Locate every cell, classifying each as a parasitized RBC, an uninfected RBC, or a WBC.
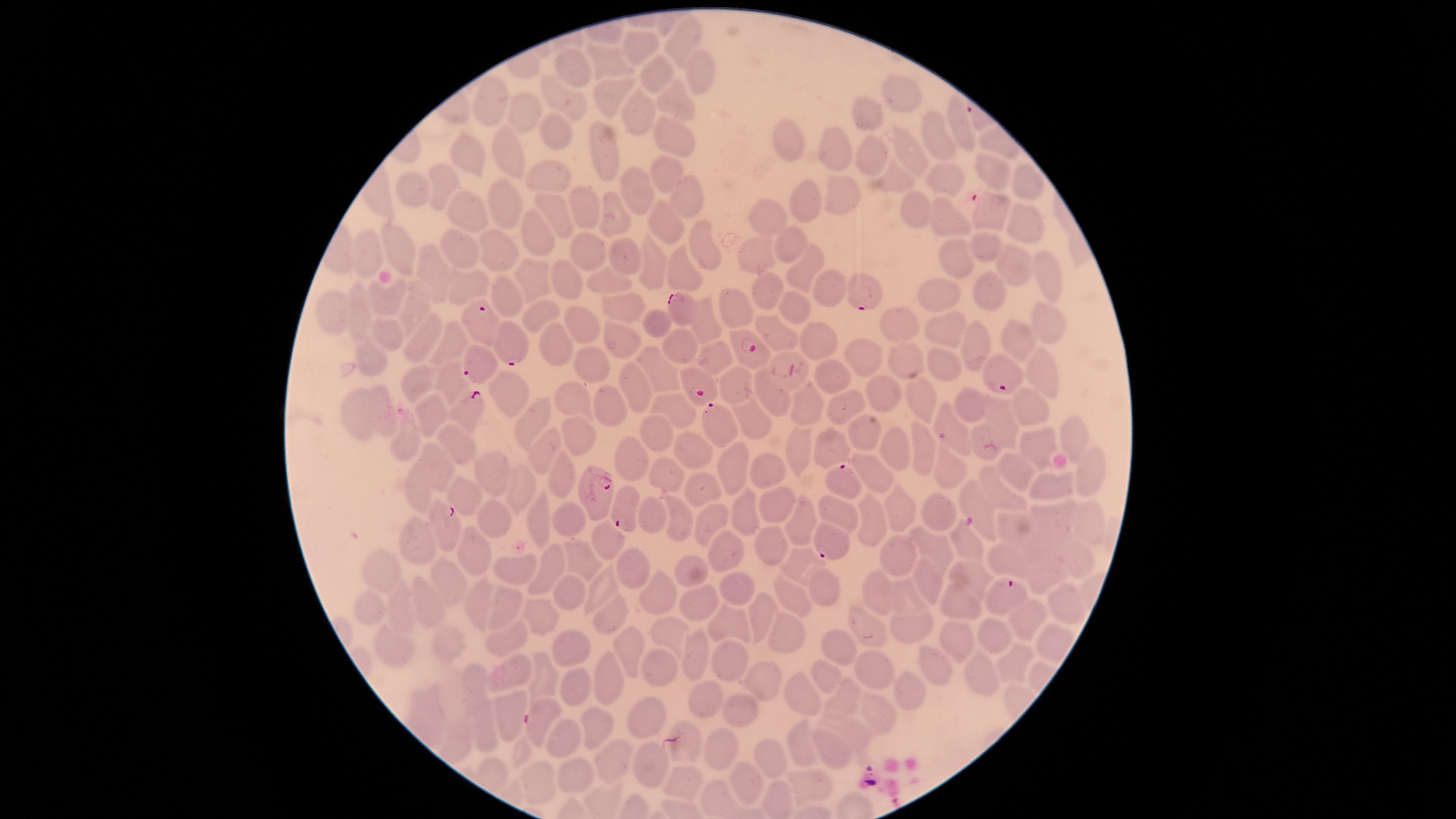

Approximate bounding boxes as (left, top, right, bottom) in pixels.
Parasitized RBCs: (845, 273, 883, 310), (666, 292, 697, 327), (461, 299, 500, 347), (493, 319, 528, 366), (729, 329, 771, 370), (462, 344, 498, 384), (982, 353, 1025, 394), (679, 365, 718, 406), (445, 390, 485, 434), (702, 403, 739, 448), (578, 464, 614, 521), (824, 464, 862, 500), (610, 486, 640, 532), (426, 498, 461, 551), (812, 522, 851, 560), (984, 578, 1028, 615), (524, 696, 563, 748).
Uninfected RBCs: (664, 15, 705, 69), (623, 30, 661, 67), (584, 42, 637, 83), (554, 48, 592, 88), (682, 49, 716, 96), (639, 52, 675, 94), (540, 71, 588, 122), (881, 72, 922, 113), (472, 73, 509, 128), (653, 75, 696, 122), (592, 77, 639, 119), (620, 84, 658, 136), (505, 91, 544, 136), (852, 95, 885, 131), (948, 95, 976, 151), (921, 109, 955, 160), (538, 111, 573, 150), (652, 114, 696, 157), (771, 118, 806, 162), (589, 120, 622, 182), (490, 122, 524, 179), (817, 124, 852, 171), (891, 124, 930, 178), (448, 129, 487, 181), (855, 132, 890, 176), (976, 151, 1012, 191), (648, 154, 685, 193), (875, 157, 916, 194), (524, 159, 572, 191), (924, 160, 966, 197), (427, 161, 461, 211), (1010, 162, 1047, 200), (619, 167, 655, 215), (395, 170, 432, 208), (823, 173, 861, 214), (669, 174, 704, 219), (789, 177, 823, 222), (486, 178, 522, 229), (567, 184, 602, 229), (972, 188, 1011, 231), (445, 189, 489, 234), (900, 189, 933, 229), (533, 191, 574, 238), (599, 191, 632, 236), (930, 195, 973, 238), (648, 199, 686, 246), (748, 199, 787, 237), (1006, 201, 1045, 246), (519, 207, 557, 255), (689, 219, 724, 271), (380, 222, 416, 276), (773, 224, 809, 264), (439, 227, 481, 268), (478, 227, 518, 273), (638, 227, 669, 290), (349, 228, 384, 279), (569, 229, 608, 270), (968, 229, 1004, 262), (736, 234, 777, 274), (607, 238, 642, 276), (938, 238, 975, 279), (993, 241, 1035, 287), (415, 242, 452, 305), (666, 243, 704, 291), (784, 243, 825, 294), (1033, 250, 1063, 305), (512, 256, 554, 304), (550, 259, 584, 299), (585, 264, 633, 294), (448, 266, 491, 306), (812, 268, 847, 307), (750, 270, 786, 309), (972, 270, 1008, 312), (490, 274, 525, 317), (366, 277, 408, 318), (396, 277, 431, 342), (917, 277, 961, 312), (345, 278, 371, 343), (718, 286, 755, 328), (315, 290, 353, 336), (600, 290, 649, 325), (777, 290, 811, 326), (690, 293, 723, 346), (521, 300, 561, 333), (1031, 301, 1068, 344), (879, 304, 919, 341), (564, 305, 600, 343), (401, 308, 443, 367), (643, 308, 674, 338), (925, 311, 969, 349), (754, 313, 800, 352), (368, 318, 403, 352), (960, 318, 992, 373), (1001, 318, 1038, 363), (424, 319, 470, 369), (603, 319, 642, 359), (799, 320, 838, 361), (538, 321, 573, 367), (661, 327, 700, 365), (354, 330, 389, 377), (843, 338, 883, 378), (886, 339, 924, 379), (693, 340, 734, 374), (927, 344, 963, 383), (633, 345, 682, 393), (573, 346, 609, 382), (1025, 346, 1062, 399), (767, 350, 812, 390), (433, 357, 470, 410), (812, 358, 851, 394), (617, 360, 654, 412), (400, 363, 435, 404), (717, 365, 755, 404), (752, 367, 792, 417), (486, 369, 530, 418), (866, 374, 903, 414), (904, 374, 940, 425), (790, 379, 826, 425), (553, 380, 594, 423), (362, 384, 397, 437), (592, 384, 628, 428), (1012, 386, 1050, 428), (952, 387, 989, 423), (339, 388, 387, 441), (414, 390, 447, 436), (826, 390, 865, 424), (649, 392, 698, 430), (982, 392, 1020, 450), (515, 395, 551, 453), (731, 395, 772, 440), (932, 401, 972, 457), (847, 413, 881, 451), (639, 415, 675, 454), (1058, 415, 1090, 463), (561, 416, 598, 459), (911, 420, 938, 476), (969, 421, 1003, 461), (390, 422, 421, 460), (435, 422, 477, 465), (527, 425, 562, 475), (1018, 425, 1058, 470), (784, 426, 814, 478), (813, 426, 851, 470), (878, 426, 911, 471), (673, 430, 714, 471), (615, 433, 651, 483), (717, 439, 749, 497), (419, 440, 456, 494), (933, 442, 968, 489), (1076, 445, 1107, 498), (546, 446, 578, 500), (474, 449, 512, 497), (998, 451, 1035, 492), (749, 452, 786, 489), (850, 453, 894, 494), (648, 457, 686, 493), (403, 461, 434, 512), (505, 463, 537, 515), (978, 464, 1029, 512), (684, 470, 722, 508), (1027, 470, 1074, 500), (445, 475, 484, 517), (884, 479, 917, 532), (959, 479, 998, 543), (729, 485, 760, 535), (758, 486, 796, 524), (526, 489, 551, 552), (856, 489, 888, 547), (784, 491, 818, 545), (920, 492, 959, 532), (664, 493, 695, 542), (636, 495, 667, 534), (816, 495, 860, 534), (477, 498, 513, 538), (550, 501, 588, 537), (1030, 501, 1076, 545), (1071, 501, 1106, 547), (693, 502, 731, 548), (997, 511, 1037, 546), (398, 516, 436, 566), (591, 518, 626, 562), (948, 519, 986, 563), (456, 524, 493, 575), (908, 524, 954, 577), (754, 525, 790, 565), (708, 529, 745, 573), (880, 534, 919, 577), (1061, 537, 1096, 580), (563, 539, 604, 584), (987, 540, 1030, 580), (526, 542, 567, 597), (779, 545, 829, 589), (615, 546, 651, 589), (361, 548, 403, 594), (492, 552, 538, 586), (1028, 552, 1070, 595), (674, 554, 709, 588), (912, 554, 942, 606), (428, 555, 467, 607), (948, 559, 995, 601), (584, 560, 619, 615), (638, 567, 679, 614), (862, 567, 894, 616), (807, 568, 840, 607), (552, 571, 588, 613), (719, 571, 755, 606), (773, 571, 813, 617), (462, 573, 491, 633), (412, 575, 445, 628), (384, 576, 418, 635), (887, 576, 931, 613), (938, 579, 984, 620), (487, 581, 526, 632), (679, 583, 720, 621), (1046, 583, 1086, 626), (354, 590, 387, 625), (592, 592, 628, 636), (746, 592, 780, 646), (1008, 597, 1047, 640), (521, 598, 560, 636), (706, 600, 752, 643), (847, 604, 888, 649), (889, 610, 935, 643), (766, 612, 807, 654), (650, 615, 691, 660), (977, 616, 1013, 654), (484, 618, 529, 660), (938, 618, 976, 662), (373, 621, 415, 665), (1035, 622, 1076, 666), (430, 625, 466, 663), (612, 625, 645, 680), (680, 626, 710, 682), (550, 627, 592, 667), (819, 628, 858, 666), (710, 639, 750, 682), (995, 641, 1036, 683), (918, 644, 954, 687), (638, 647, 679, 687), (963, 647, 999, 697), (853, 649, 895, 690), (592, 650, 624, 706), (525, 651, 560, 702), (490, 654, 535, 693), (811, 659, 843, 694), (742, 661, 784, 702), (456, 663, 492, 713), (559, 666, 593, 706), (892, 669, 926, 712), (782, 670, 821, 716), (822, 677, 862, 717), (687, 680, 723, 718), (403, 686, 448, 748), (493, 689, 529, 741), (721, 690, 759, 729), (857, 690, 897, 735), (627, 695, 668, 740), (468, 698, 499, 752), (580, 705, 614, 750), (815, 715, 874, 752), (437, 716, 475, 764), (786, 716, 819, 767), (545, 718, 581, 760), (663, 719, 703, 763), (703, 726, 739, 772), (809, 727, 854, 770), (594, 737, 636, 783), (754, 738, 788, 778), (631, 741, 670, 788), (556, 757, 595, 794), (728, 759, 763, 807), (519, 760, 560, 805), (662, 763, 705, 801), (783, 767, 833, 808).
No WBCs identified.

visible region = circular
stain = Giemsa
field of view = single
species = Plasmodium falciparum
image size = 1456×819 pixels
capture = smartphone photograph through the microscope eyepiece
preparation = thin blood smear